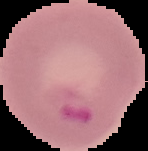
Summary:
  - Image size: 148×151 pixels
  - Image type: segmented cell region with the area outside set to black
  - Preparation: thin blood smear
  - Malaria status: parasitized